Classify this cell by malaria status.
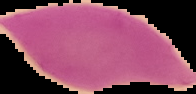
Uninfected.

Summary:
  - Image type: segmented cell region on a black background
  - Image size: 196×94 pixels
  - Preparation: thin blood smear